Identify the cell.
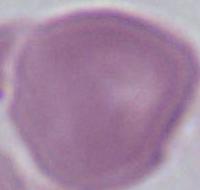

An erythrocyte.

{
  "magnification": "1000x",
  "modality": "micrograph"
}